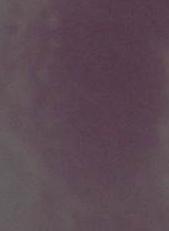

{
  "identification": "erythrocyte",
  "modality": "micrograph",
  "magnification": "1000x"
}